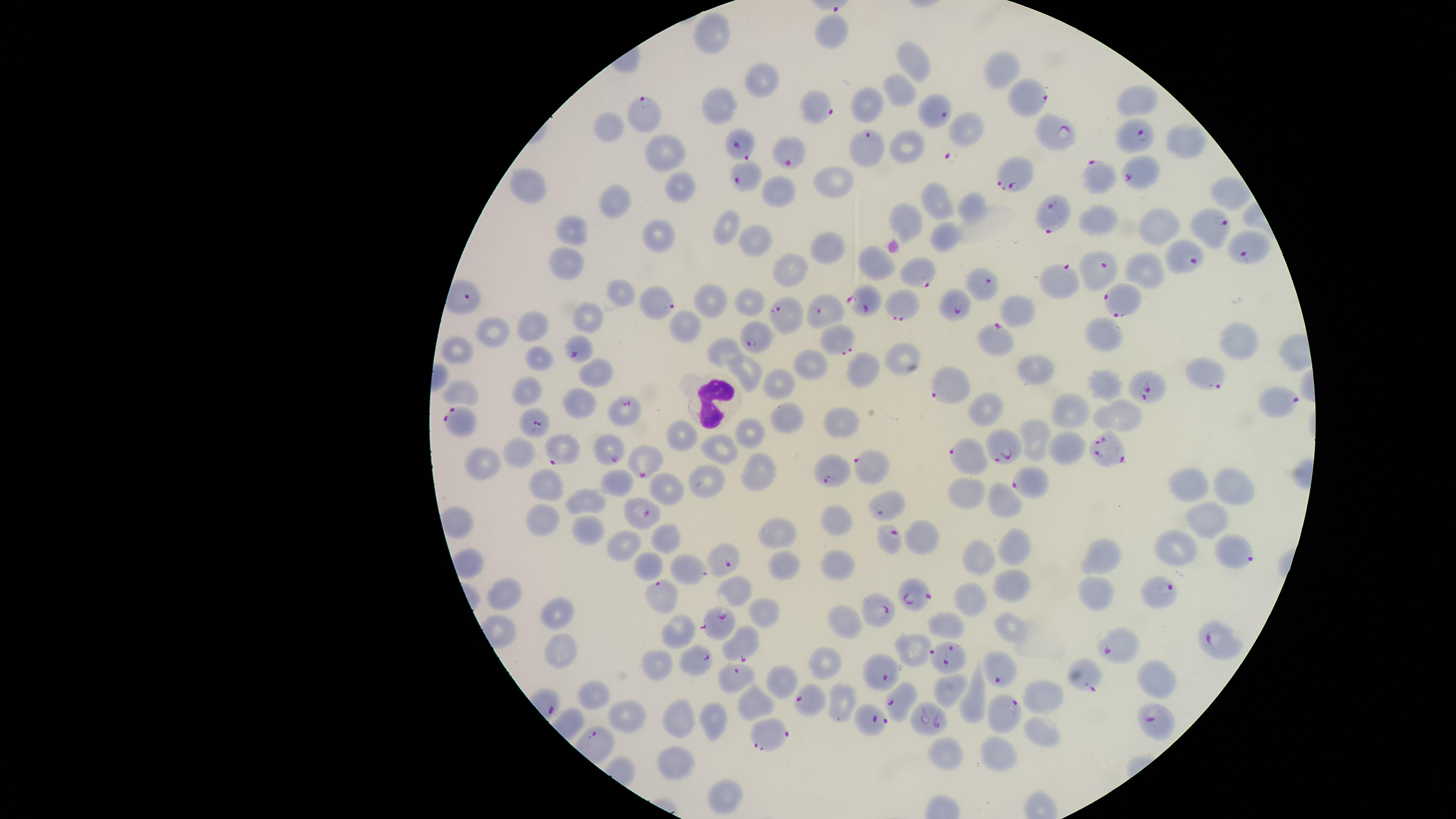

visible_region: circular
uninfected_red_blood_cells: 'approximate marker points as (x, y) in pixels: (830, 34), (714, 36), (913, 60), (1001, 67), (761, 81), (898, 93), (721, 103), (1135, 103), (865, 105), (613, 126), (966, 130), (905, 139), (1174, 139), (662, 148), (834, 183), (525, 184), (680, 187), (777, 189), (1225, 190), (619, 200), (937, 205), (971, 205), (1154, 218), (909, 220), (729, 227), (574, 232), (655, 233), (946, 234), (749, 239), (826, 247), (876, 262), (788, 266), (561, 268), (1146, 270), (619, 291), (709, 302), (749, 302), (1017, 310), (587, 313), (538, 324), (1106, 328), (680, 329), (493, 333), (1234, 338), (725, 349), (899, 353), (459, 355), (537, 360), (806, 360), (740, 367), (595, 369), (1036, 369), (862, 371), (782, 380), (1105, 382), (521, 390), (464, 394), (580, 401), (985, 406), (1072, 410), (1115, 414), (842, 419), (789, 422), (746, 430), (1032, 435), (684, 437), (1063, 446), (718, 448), (520, 457), (483, 462), (760, 473), (1186, 480), (616, 483), (701, 483), (668, 487), (1235, 487), (545, 490), (966, 490), (1002, 497), (584, 501), (1206, 515), (831, 519), (543, 521), (585, 531), (778, 531), (924, 535), (664, 536), (625, 542), (1178, 544), (1015, 546), (977, 556), (1104, 559), (783, 563), (838, 565), (646, 567), (1014, 582), (510, 593), (976, 593), (1092, 593), (737, 594), (761, 615), (557, 616), (846, 620), (955, 624), (1012, 624), (676, 629), (918, 644), (563, 651), (826, 663), (657, 664), (1154, 672), (782, 681), (953, 690), (1044, 695), (594, 700), (974, 701), (753, 706), (841, 706), (677, 717), (714, 721), (629, 722), (1038, 737), (947, 750), (1004, 757), (679, 766), (719, 796)'
stain: Giemsa
presence: malaria parasites seen
parasitized_red_blood_cells: 'approximate marker points as (x, y) in pixels: (1030, 99), (818, 109), (932, 110), (646, 113), (1131, 136), (1053, 137), (738, 142), (869, 147), (792, 153), (1138, 169), (1014, 174), (746, 178), (1094, 178), (1052, 214), (1205, 223), (1250, 248), (1185, 258), (1101, 269), (919, 270), (1062, 280), (983, 283), (652, 301), (1121, 301), (865, 302), (957, 306), (902, 308), (824, 311), (782, 312), (753, 338), (996, 340), (836, 342), (578, 349), (1208, 378), (946, 386), (1149, 388), (1283, 401), (628, 408), (459, 419), (533, 422), (610, 450), (1107, 450), (1000, 451), (566, 453), (967, 453), (648, 462), (867, 463), (830, 467), (1030, 481), (885, 507), (643, 512), (890, 542), (1231, 554), (726, 556), (695, 568), (918, 591), (1160, 595), (662, 597), (882, 613), (717, 624), (1216, 641), (741, 647), (1122, 648), (699, 656), (944, 660), (878, 674), (999, 675), (1084, 679), (736, 682), (895, 697), (814, 702), (1005, 712), (931, 718), (1153, 719), (874, 720), (774, 734)'
preparation: thin blood smear
image_size: 1456×819 pixels
field_of_view: single
capture: smartphone photograph through the microscope eyepiece
species: Plasmodium falciparum
white_blood_cells: 'approximate marker points as (x, y) in pixels: (712, 401)'